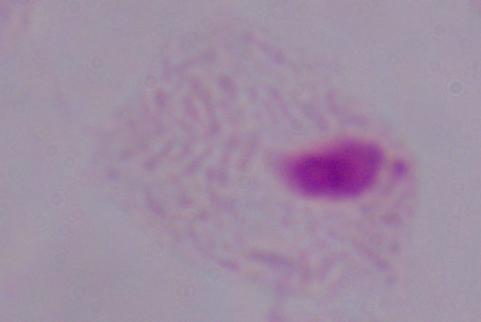 Micrograph. A trichomonad is seen. 1000x magnification.